Give a bounding box for every malaria parasite.
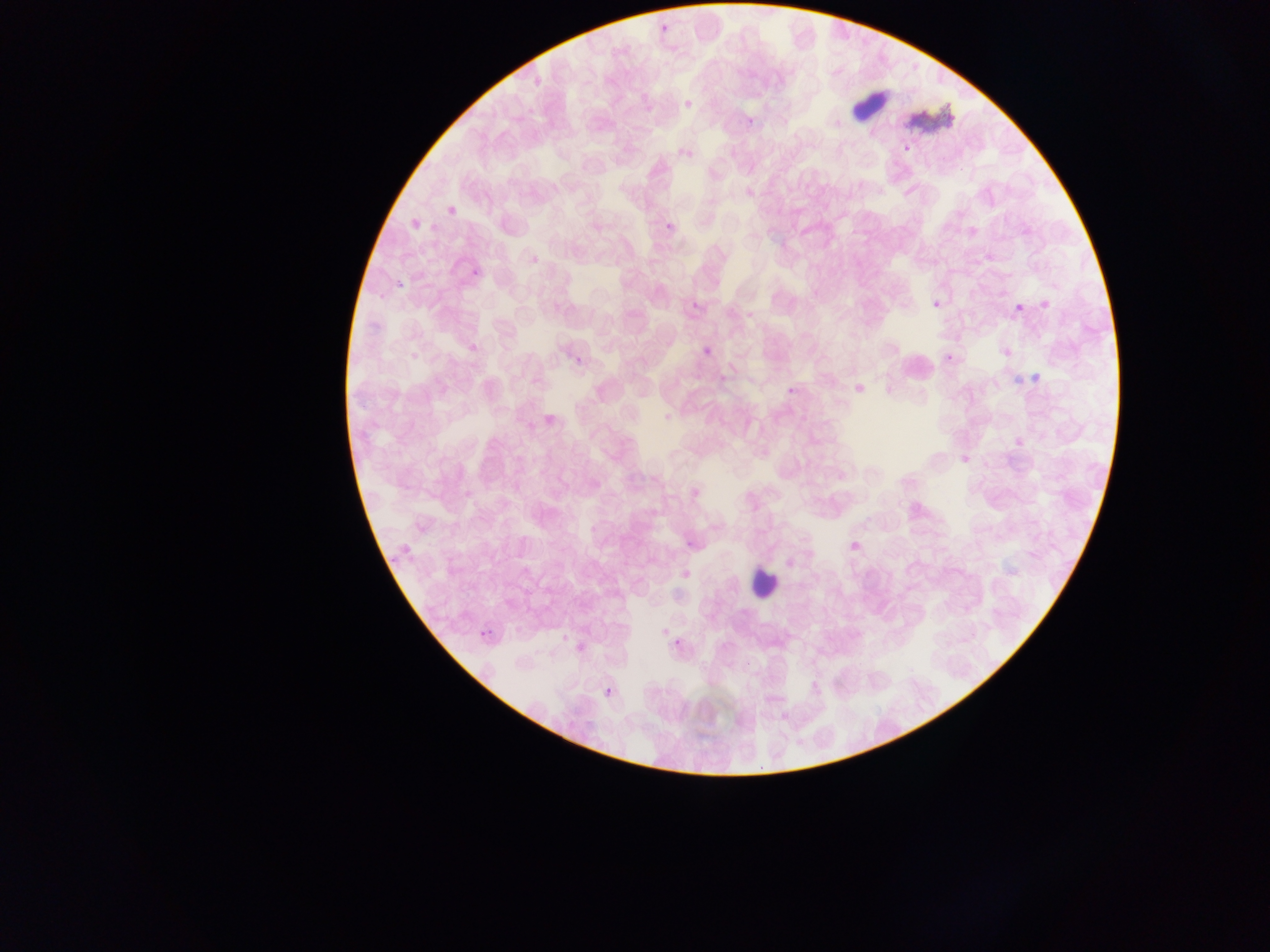
Approximate bounding boxes as left top right bottom in pixels.
Malaria parasites: 657 20 674 33; 684 99 695 110; 743 117 757 123; 904 144 912 153; 661 219 677 233; 469 266 482 278; 392 280 404 289; 691 301 700 309; 933 301 942 309; 1012 301 1022 311; 705 345 717 353; 948 349 956 363; 571 351 586 368; 1033 364 1044 388; 1013 374 1023 382; 785 380 799 394; 681 535 695 551; 383 554 396 569; 478 628 487 640; 673 642 684 648; 605 684 613 697.

Summary:
  - Leukocyte locations: 747 562 781 599
  - Artifact (stain precipitate or debris) locations: 847 80 891 125; 909 101 957 134
  - Preparation: thin blood film
  - Country: Ghana
  - Capture: mobile-phone photograph through a microscope
  - Image size: 1270×952 pixels
  - Field of view: single